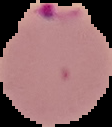 Malaria status: parasitized. From a thin blood smear. Image is 112×127 pixels. Cell region segmented out of the field of view; the surrounding area is masked to black.